Assess this cell for malaria.
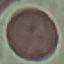
It is uninfected.

Summary:
  - Stain: Giemsa
  - Preparation: thin blood film
  - Capture: smartphone camera at the microscope eyepiece
  - Image type: automatically extracted cell patch, resized to 64 × 64 pixels